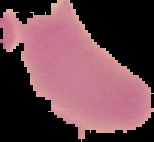

{
  "preparation": "thin blood film",
  "image_type": "segmented cell region on a black background",
  "malaria_status": "uninfected",
  "image_size": "154×142 pixels"
}